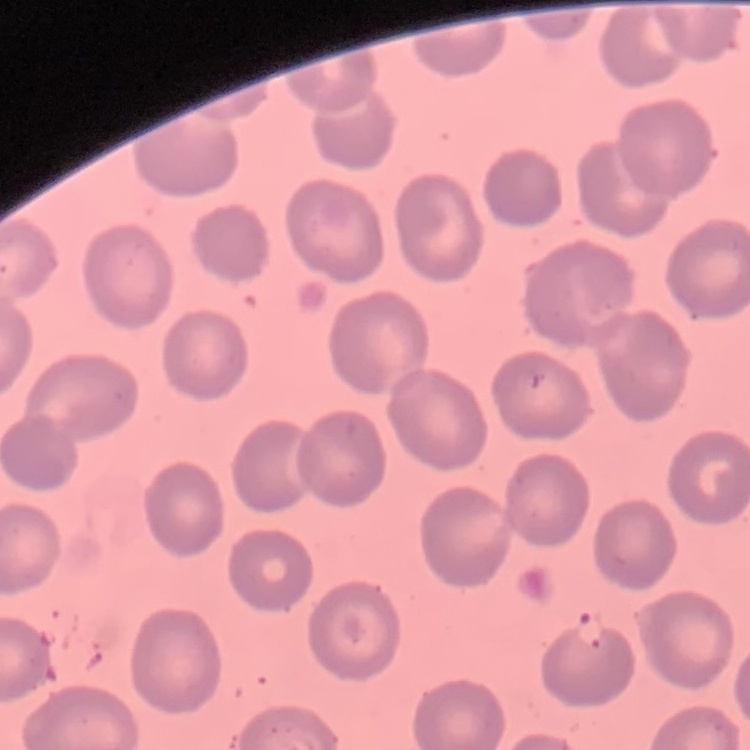

The erythrocytes exhibit no rouleaux formation. Thin blood smear. Field's or Giemsa stain. Square crop of a larger photomicrograph.